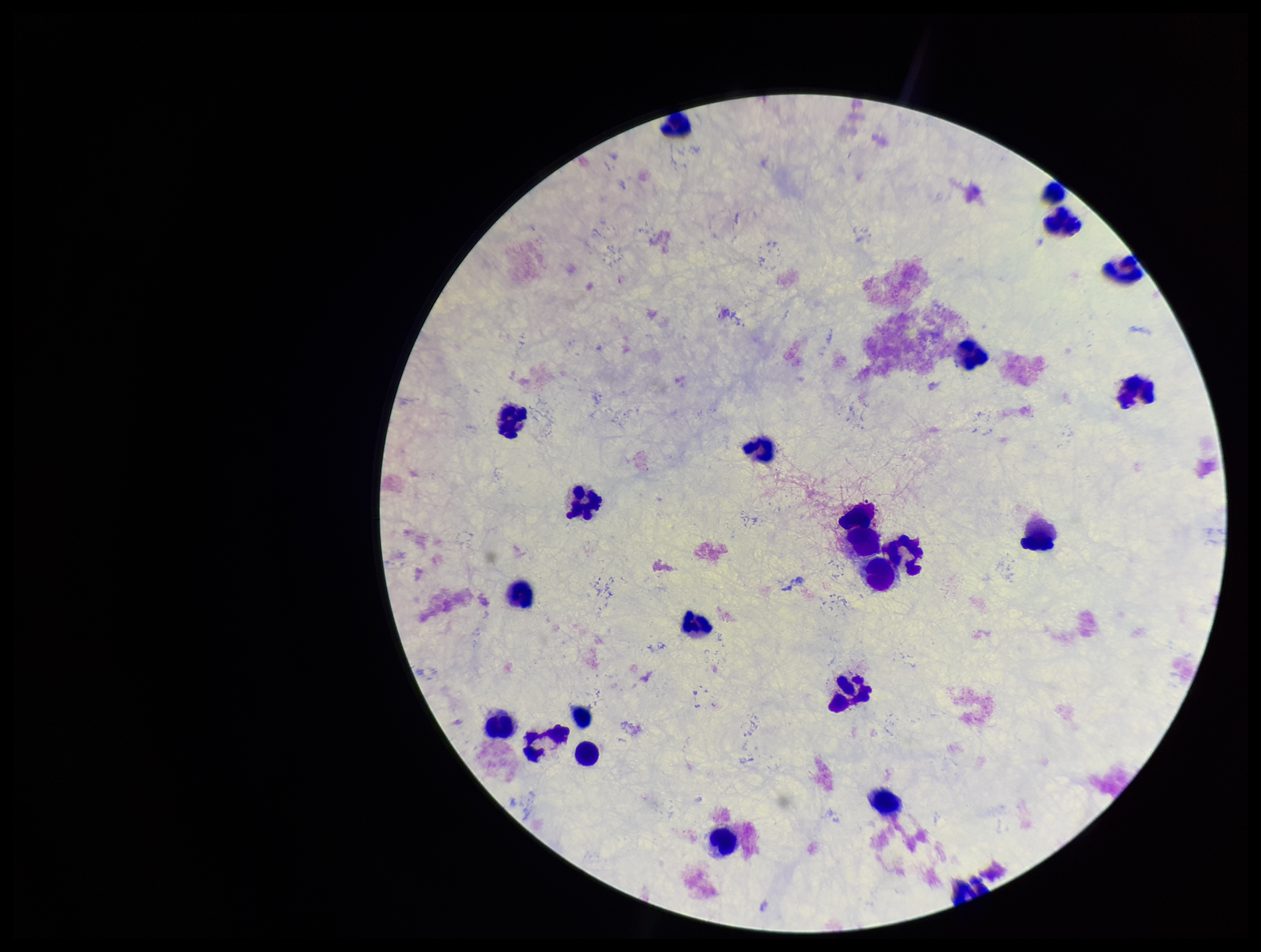
Giemsa stain. Image is 1261×952 pixels. Single field of view. Parasite count: 0. Patient malaria status: negative. Leukocyte count: 23. Plasmodium parasites: none seen. Smartphone photograph taken through the eyepiece of a microscope. Preparation: thick.